Classify this cell by malaria status.
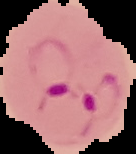

Parasitized.

Summary:
  - Image size: 136×154 pixels
  - Image type: segmented cell region on a black background
  - Preparation: thin blood smear